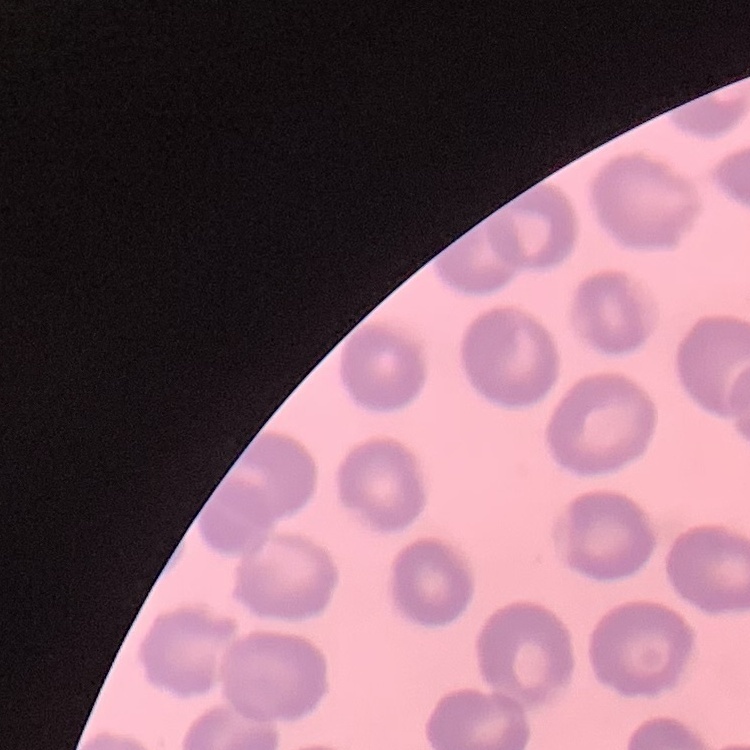
The red blood cells show no rouleaux formation. Thin blood smear. One tile cut from a larger photomicrograph. Stained with either Field's or Giemsa.